State the preparation type.
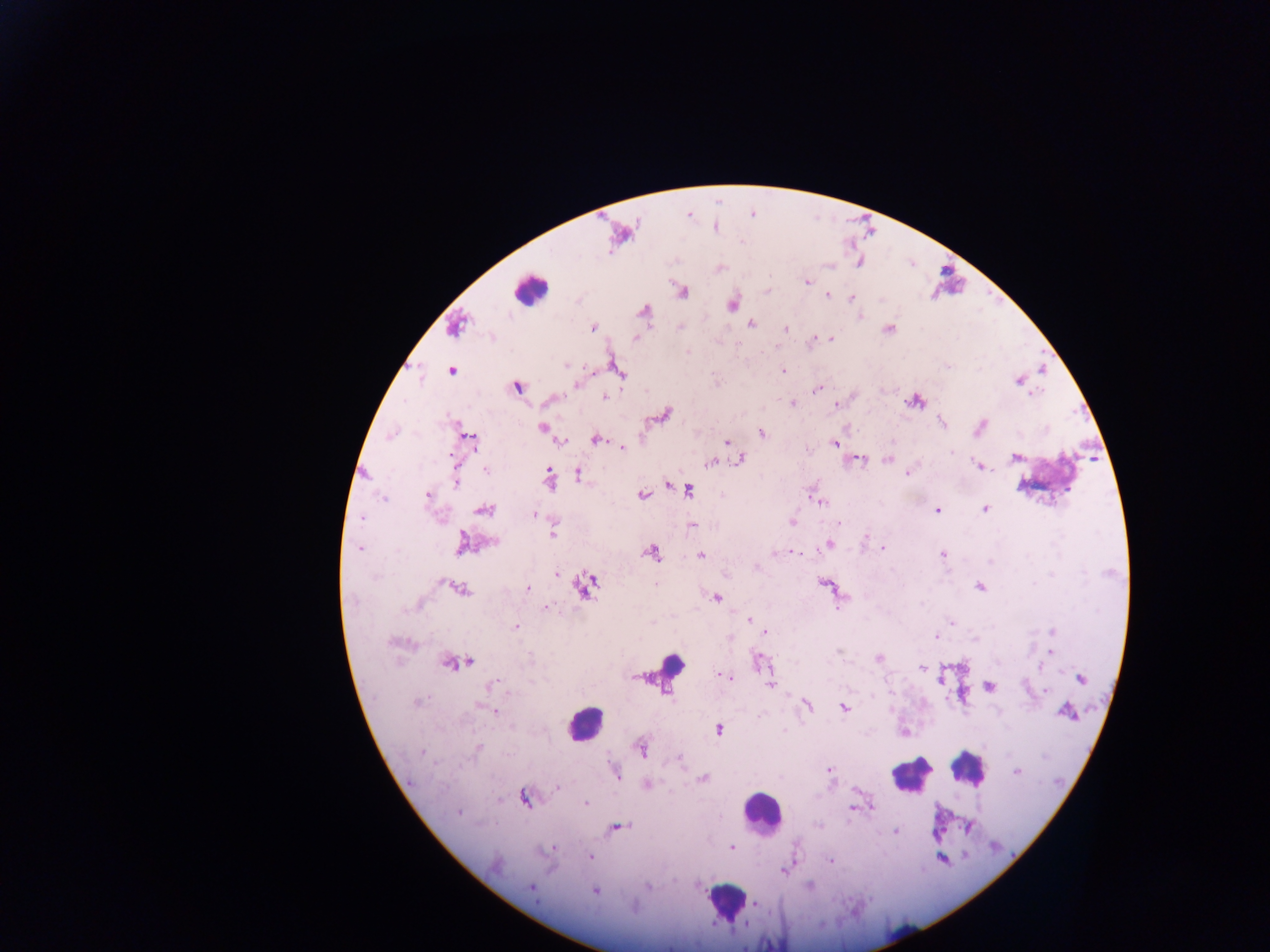
Thick blood film.

country = Ghana
field of view = single
capture = mobile-phone photograph through a microscope
image size = 1270×952 pixels
malaria parasite locations = approximate centers as x y in pixels: 807 282; 828 295; 851 298; 732 303; 860 317; 751 323; 593 327; 680 328; 785 328; 889 328; 815 338; 635 339; 831 339; 565 366; 783 370; 451 371; 592 372; 1019 380; 576 385; 517 387; 818 389; 1031 393; 605 397; 915 402; 793 403; 836 405; 942 422; 982 424; 541 428; 762 433; 390 435; 471 439; 596 439; 560 443; 727 443; 835 444; 623 449; 951 453; 1014 457; 741 460; 887 460; 860 461; 711 464; 977 465; 485 469; 579 474; 908 474; 549 479; 455 482; 668 487; 688 490; 428 495; 641 495; 383 499; 821 502; 986 509; 484 510; 938 510; 533 514; 361 518; 792 522; 840 522; 694 525; 552 533; 866 538; 493 542; 462 543; 829 544; 360 549; 883 549; 652 553; 793 553; 700 555; 942 555; 989 562; 757 569; 557 574; 656 584; 823 584; 584 585; 979 587; 527 588; 461 589; 717 597; 837 606; 545 608; 749 619; 952 622; 516 626; 1052 631; 765 633; 730 637; 936 637; 392 642; 1051 651; 838 652; 878 658; 758 660; 469 662; 448 664; 921 668; 1039 668; 725 676; 1081 679; 496 684; 771 684; 988 687; 1046 691; 417 702; 808 705; 480 706; 843 708; 492 711; 1067 712; 719 729; 477 748; 641 749; 422 752; 679 758; 829 771; 616 772; 1017 772; 702 778; 647 784; 557 787; 525 798; 586 803; 853 809; 459 812; 818 825; 617 827; 894 831; 731 847; 554 849; 590 857; 830 861; 784 871; 809 886; 647 887; 531 888; 595 891; 754 903
leukocyte locations = approximate centers as x y in pixels: 529 290; 671 663; 584 723; 969 766; 910 775; 763 811; 725 901